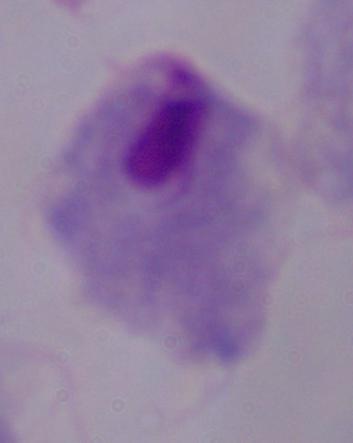
{
  "modality": "micrograph",
  "identification": "trichomonad",
  "magnification": "1000x"
}